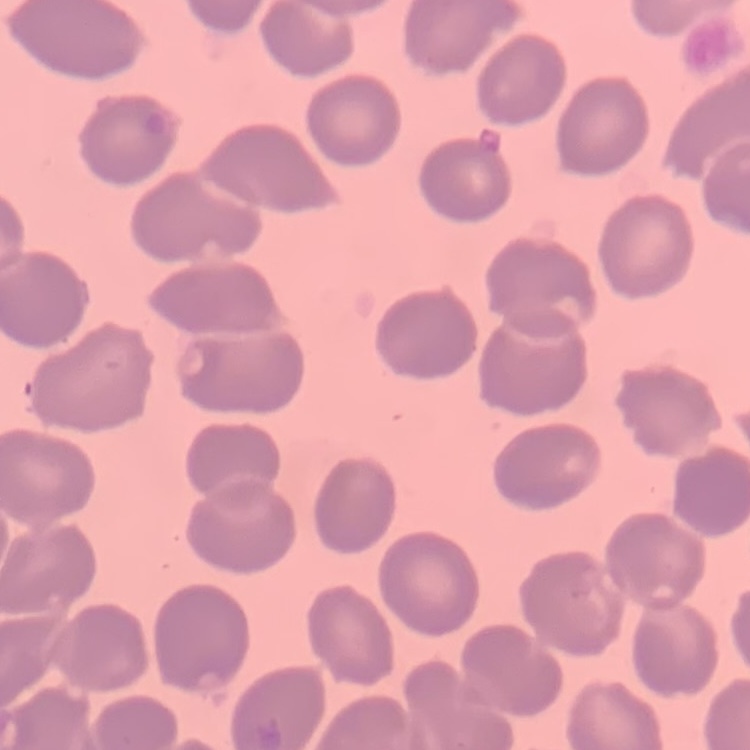

Summary:
  - Red blood cell morphology: no rouleaux formation
  - Image type: one tile cut from a larger photomicrograph
  - Stain: Field's or Giemsa
  - Preparation: thin peripheral smear